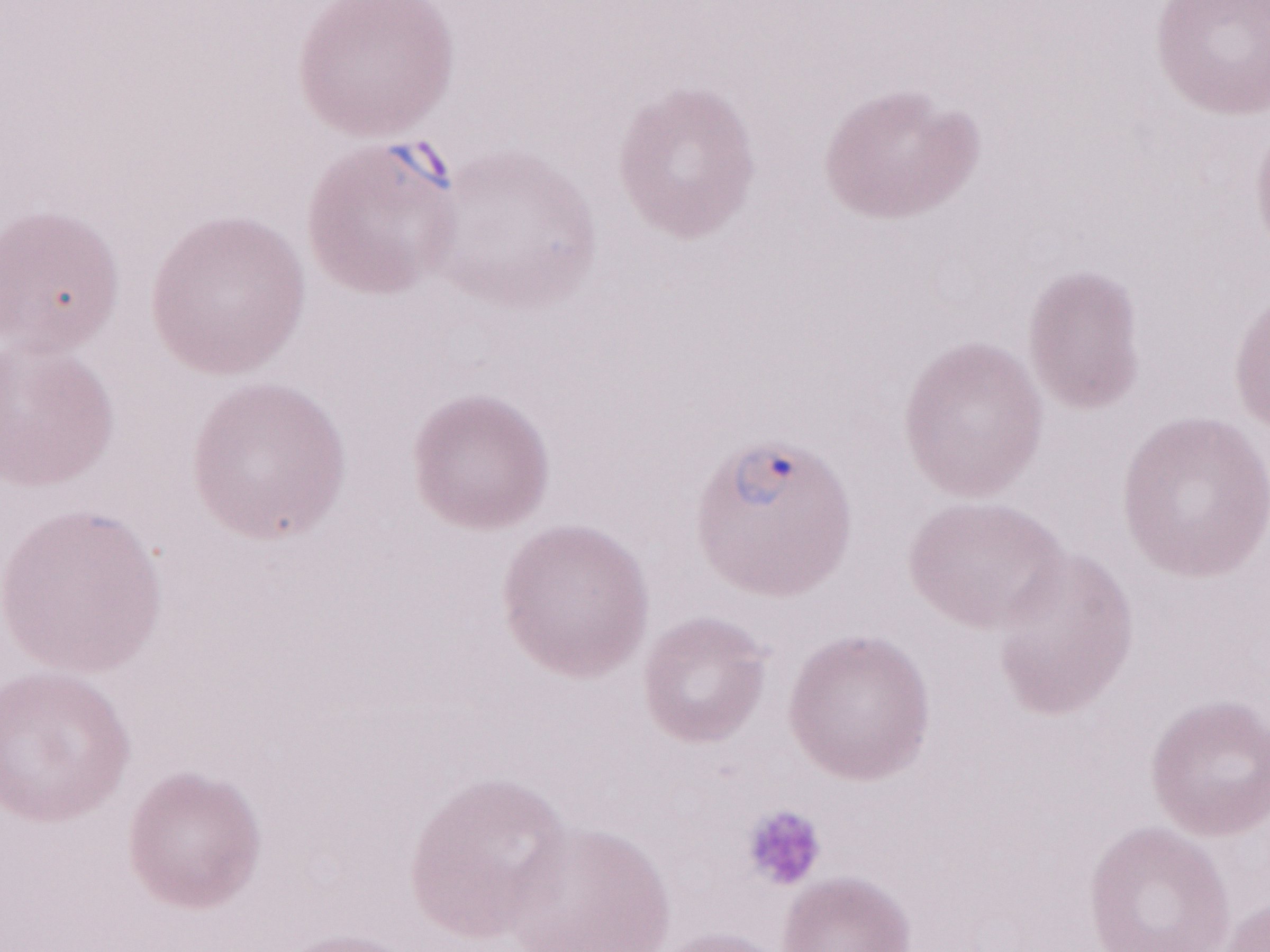

Thin blood smear. Malaria diagnosis (patient-level): positive. May-Grünwald-Giemsa (MGG) stain. Single field of view. Image is 1270×952 pixels. Magnification: 1,000x. Olympus BX43 microscope, Olympus DP73 camera.